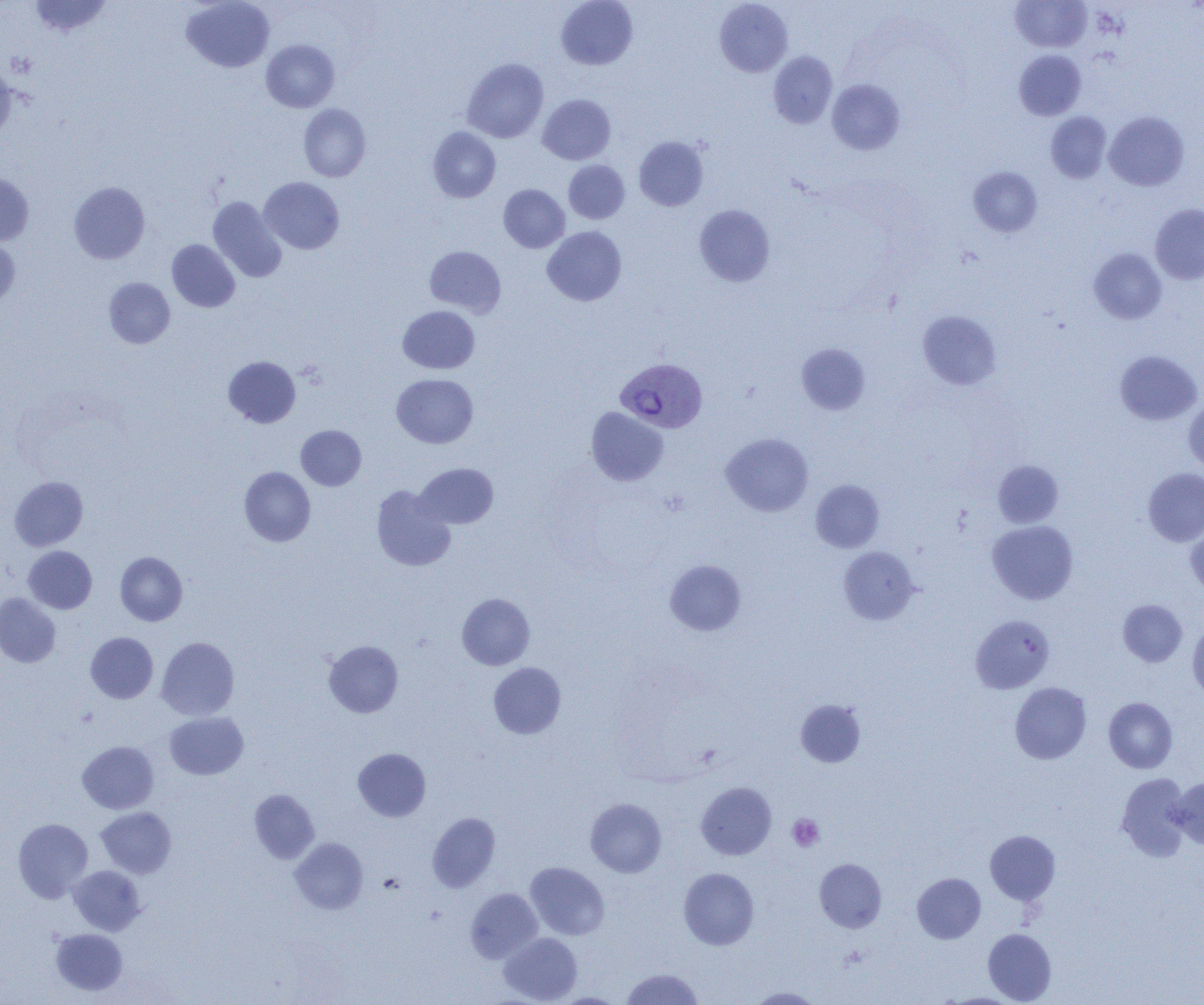
Approximate bounding boxes as (x1, y1, x2, y2) in pixels. Plasmodium vivax-infected red blood cell locations: (615, 358, 707, 433). Platelet locations: (787, 814, 824, 851). Uninfected red blood cell locations: (29, 0, 112, 37), (181, 0, 274, 72), (556, 0, 638, 70), (714, 0, 793, 77), (1011, 0, 1092, 52), (261, 39, 339, 112), (1014, 50, 1086, 120), (768, 51, 838, 128), (461, 58, 549, 143), (0, 63, 16, 141), (827, 79, 905, 155), (538, 94, 616, 164), (298, 104, 371, 182), (1104, 111, 1189, 191), (1046, 112, 1112, 183), (427, 126, 501, 203), (634, 136, 708, 211), (563, 160, 630, 224), (968, 166, 1042, 237), (0, 170, 34, 246), (258, 177, 345, 254), (69, 181, 150, 264), (498, 184, 570, 253), (208, 196, 287, 283), (694, 204, 775, 287), (1150, 204, 1204, 284), (542, 226, 627, 306), (0, 238, 20, 310), (167, 240, 240, 312), (424, 245, 506, 317), (1089, 248, 1167, 324), (103, 277, 175, 348), (398, 305, 480, 374), (918, 310, 1002, 390), (797, 344, 870, 414), (1115, 350, 1202, 425), (223, 356, 300, 428), (391, 374, 478, 448), (1183, 400, 1204, 474), (586, 407, 668, 486), (296, 425, 366, 490), (721, 432, 813, 516), (992, 460, 1063, 528), (415, 463, 498, 529), (239, 467, 316, 546), (1143, 468, 1204, 546), (9, 476, 88, 550), (811, 480, 884, 552), (371, 485, 456, 571), (987, 520, 1078, 604), (1186, 520, 1204, 596), (23, 546, 97, 614), (838, 547, 919, 624), (115, 552, 187, 626), (665, 559, 746, 635), (0, 593, 61, 668), (457, 593, 535, 670), (1118, 599, 1187, 666), (971, 615, 1054, 693), (1187, 620, 1204, 701), (86, 632, 158, 703), (156, 636, 239, 720), (323, 640, 403, 718), (488, 662, 566, 739), (1010, 682, 1091, 764), (1104, 697, 1177, 773), (795, 699, 866, 768), (165, 712, 248, 779), (77, 741, 158, 814), (353, 748, 431, 821), (1116, 773, 1191, 860), (1170, 776, 1204, 849), (696, 782, 777, 860), (249, 789, 320, 864), (585, 798, 666, 877), (96, 807, 176, 878), (427, 812, 500, 892), (13, 818, 93, 902), (985, 830, 1060, 905), (290, 837, 368, 914), (815, 858, 887, 932), (525, 862, 610, 940), (68, 865, 145, 935), (679, 868, 759, 949), (912, 873, 986, 943), (466, 888, 543, 963), (51, 928, 127, 996), (983, 928, 1056, 1004), (499, 932, 583, 1004), (621, 968, 704, 1004), (746, 987, 823, 1004), (550, 992, 627, 1004), (941, 993, 1023, 1005). Slide-level diagnosis: Plasmodium vivax. Thin blood smear. Image is 1204×1005 pixels. Optical microscopy. Captured at 1000x magnification. Single field of view.